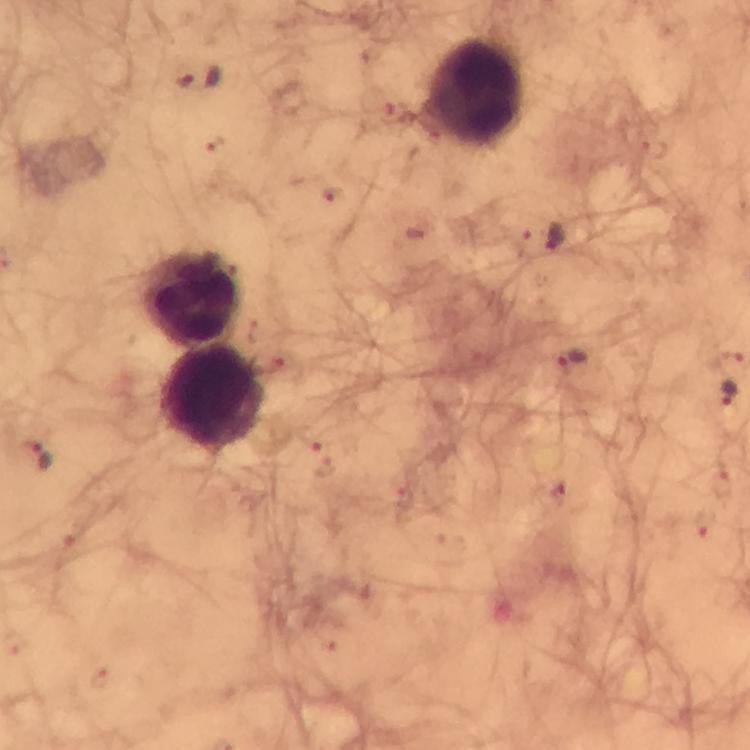

leukocyte locations = approximate centers as {x, y} in pixels: {478, 90}, {192, 296}, {209, 397}
capture = smartphone camera through the microscope
Plasmodium parasite locations = approximate centers as {x, y} in pixels: {200, 78}, {552, 235}, {570, 357}, {727, 392}, {37, 455}
stain = Giemsa
cropped from = one field of view
image size = 750×750 pixels
preparation = thick blood film
immersion oil = used
context = from a malaria diagnostic workup
magnification = 100x